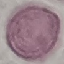
result = no malaria parasites seen
preparation = thin blood film
capture = smartphone camera at the microscope eyepiece
stain = Giemsa
image type = automatically extracted cell patch, resized to 64 × 64 pixels